Assess the morphology of the red blood cells.
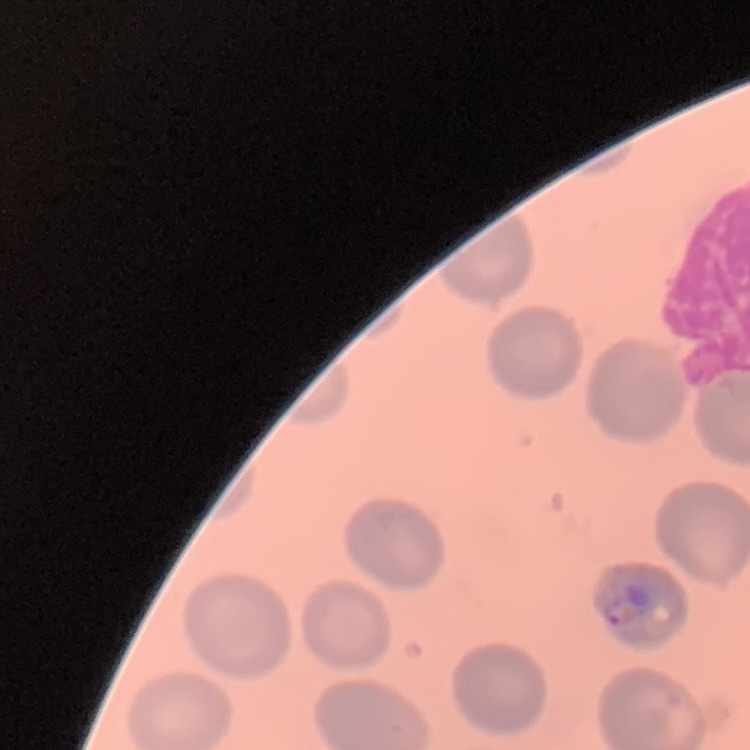

No rouleaux formation.

One tile cut from a larger photomicrograph. Stained with either Field's or Giemsa. Thin peripheral smear.